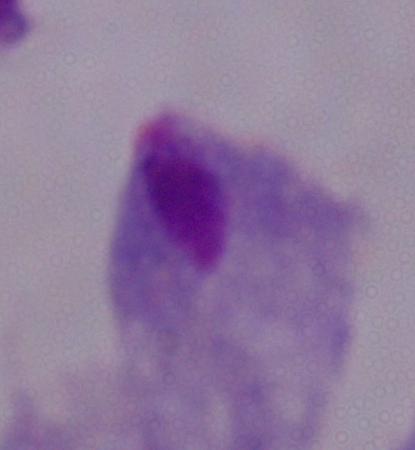
A trichomonad is seen. Micrograph. Captured at 1000x magnification.